Assess the morphology of the red blood cells.
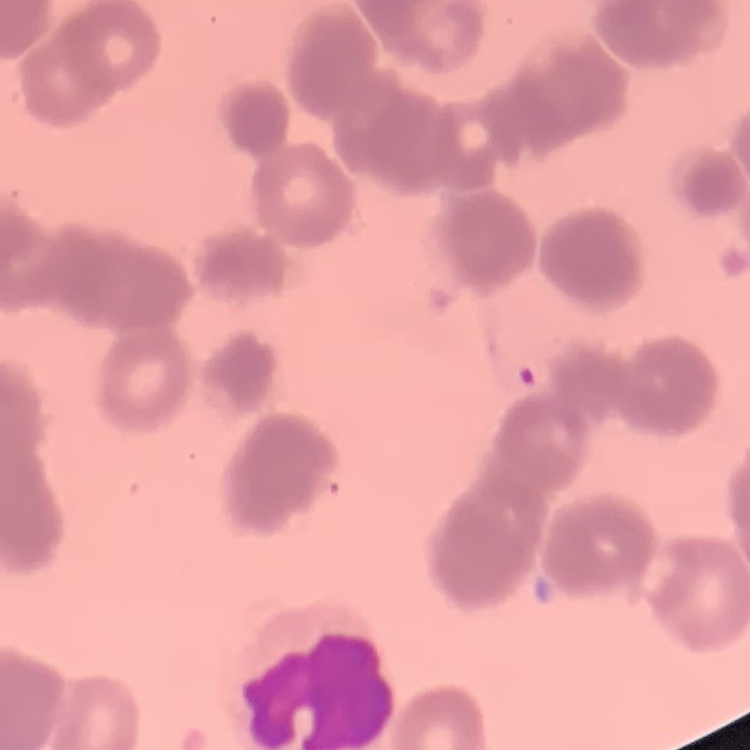

They show rouleaux formation.

stain: Field's or Giemsa
preparation: thin blood smear
image_type: one tile cut from a larger photomicrograph